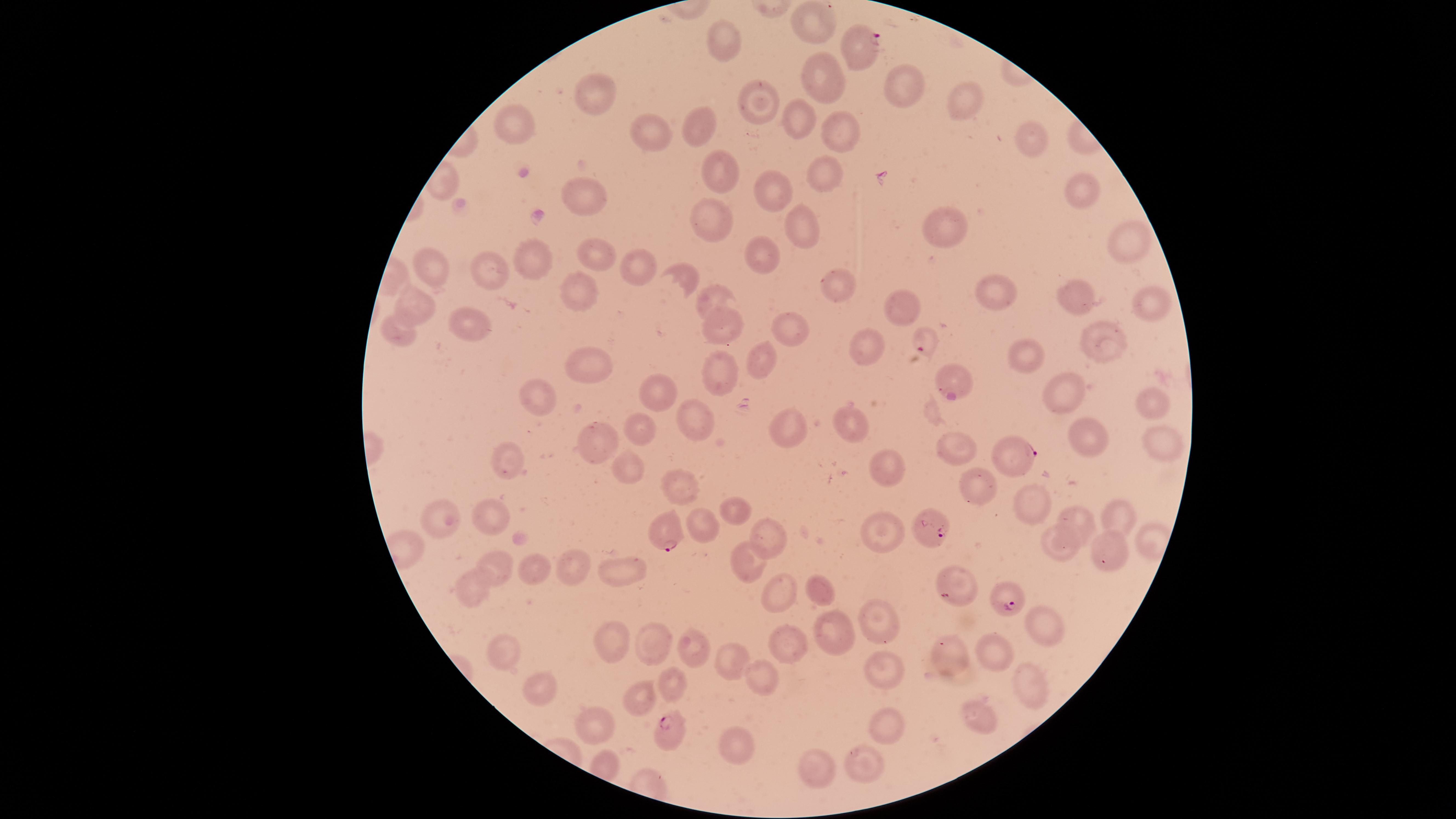

presence = malaria parasites detected
uninfected RBCs = approximate marker points as (x, y) in pixels: (813, 26), (728, 47), (821, 86), (596, 88), (904, 94), (762, 100), (964, 107), (795, 119), (695, 126), (515, 127), (657, 129), (838, 129), (1032, 136), (824, 166), (716, 172), (1084, 188), (774, 193), (585, 199), (711, 216), (945, 222), (802, 230), (1128, 241), (767, 257), (542, 259), (584, 260), (489, 262), (638, 268), (423, 270), (681, 273), (837, 284), (998, 288), (1080, 292), (713, 295), (577, 296), (1152, 299), (416, 302), (905, 303), (469, 323), (791, 326), (725, 331), (401, 334), (1103, 342), (870, 347), (752, 355), (1031, 355), (592, 370), (721, 373), (951, 378), (1062, 392), (662, 393), (532, 394), (1145, 399), (853, 416), (699, 423), (791, 426), (638, 431), (600, 441), (952, 443), (507, 467), (890, 469), (978, 486), (683, 488), (1024, 498), (733, 508), (443, 513), (489, 513), (1112, 515), (1083, 524), (705, 528), (889, 530), (776, 532), (1052, 550), (1106, 553), (746, 558), (492, 566), (573, 568), (622, 568), (535, 573), (778, 578), (958, 588), (471, 590), (827, 595), (1035, 625), (880, 627), (837, 630), (609, 637), (653, 638), (693, 648), (503, 649), (796, 651), (729, 654), (997, 654), (952, 656), (888, 666), (668, 680), (764, 680), (1024, 681), (540, 685), (646, 703), (977, 720), (883, 723), (604, 726), (735, 740), (861, 756), (820, 769)
preparation = thin blood smear
parasitized RBCs = approximate marker points as (x, y) in pixels: (863, 41), (925, 340), (1014, 461), (666, 530), (933, 532), (1004, 600), (670, 727)
image size = 1456×819 pixels
species = Plasmodium falciparum
visible region = circular
stain = Giemsa
capture = smartphone photograph through the microscope eyepiece
field of view = single